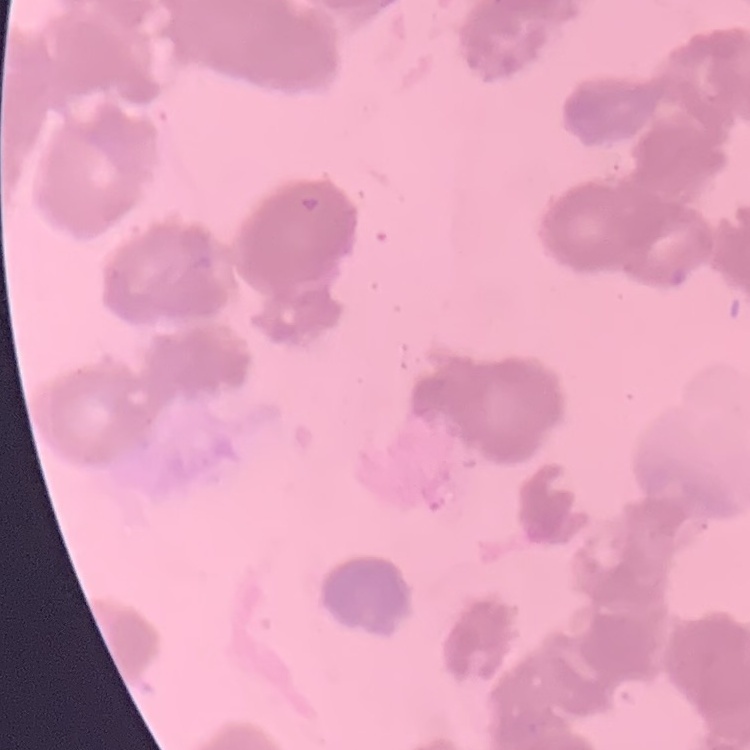
Summary:
  - Red blood cell morphology: rouleaux formation
  - Image type: square crop of a larger photomicrograph
  - Stain: Field's or Giemsa
  - Preparation: thin peripheral smear